Identify the preparation type.
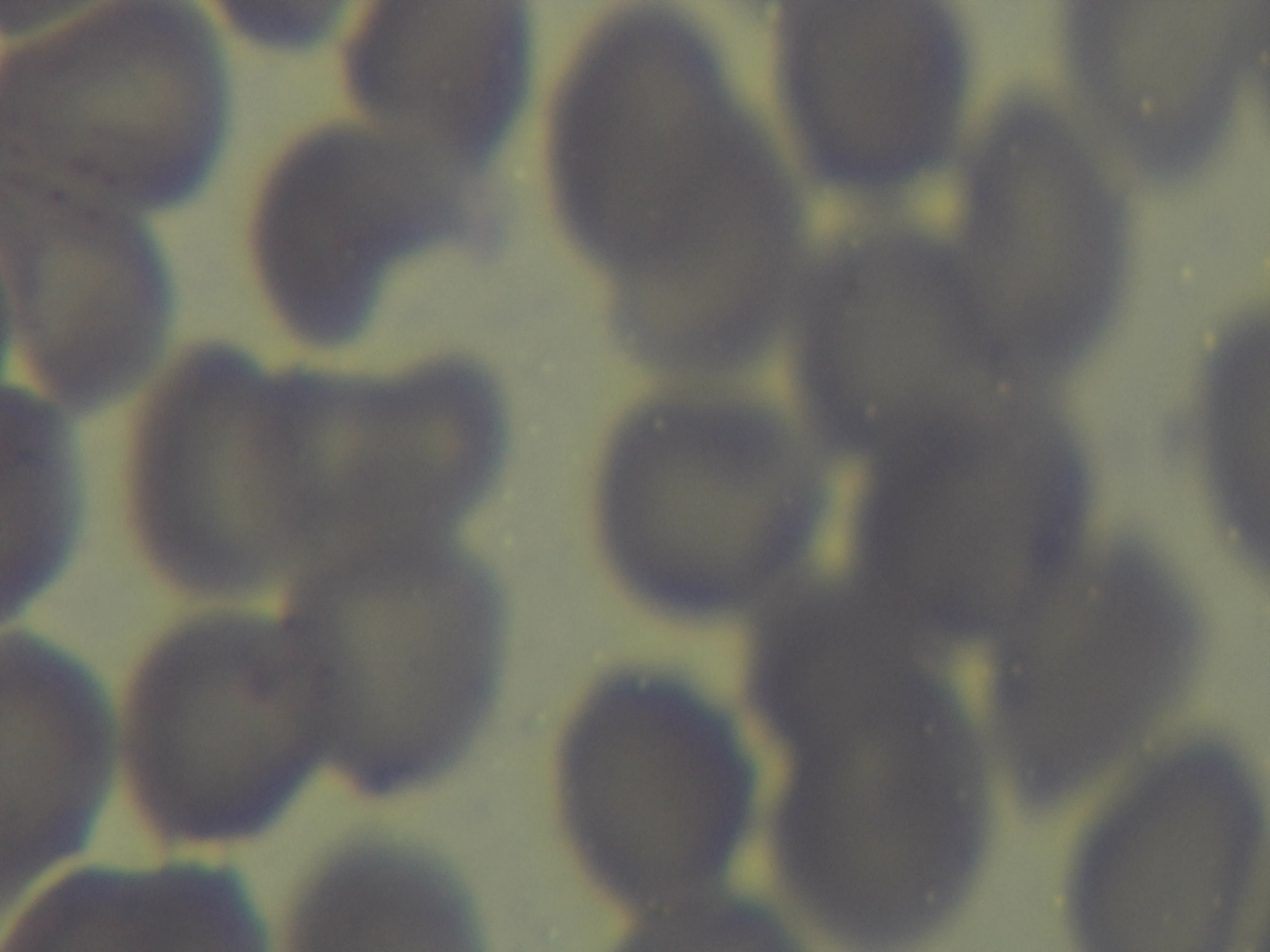
Thin.

{
  "field_of_view": "one from the slide",
  "modality": "light microscopy",
  "stain": "Giemsa",
  "capture": "mounted 4K digital camera",
  "objective": "100x oil immersion",
  "malaria_status": "uninfected"
}